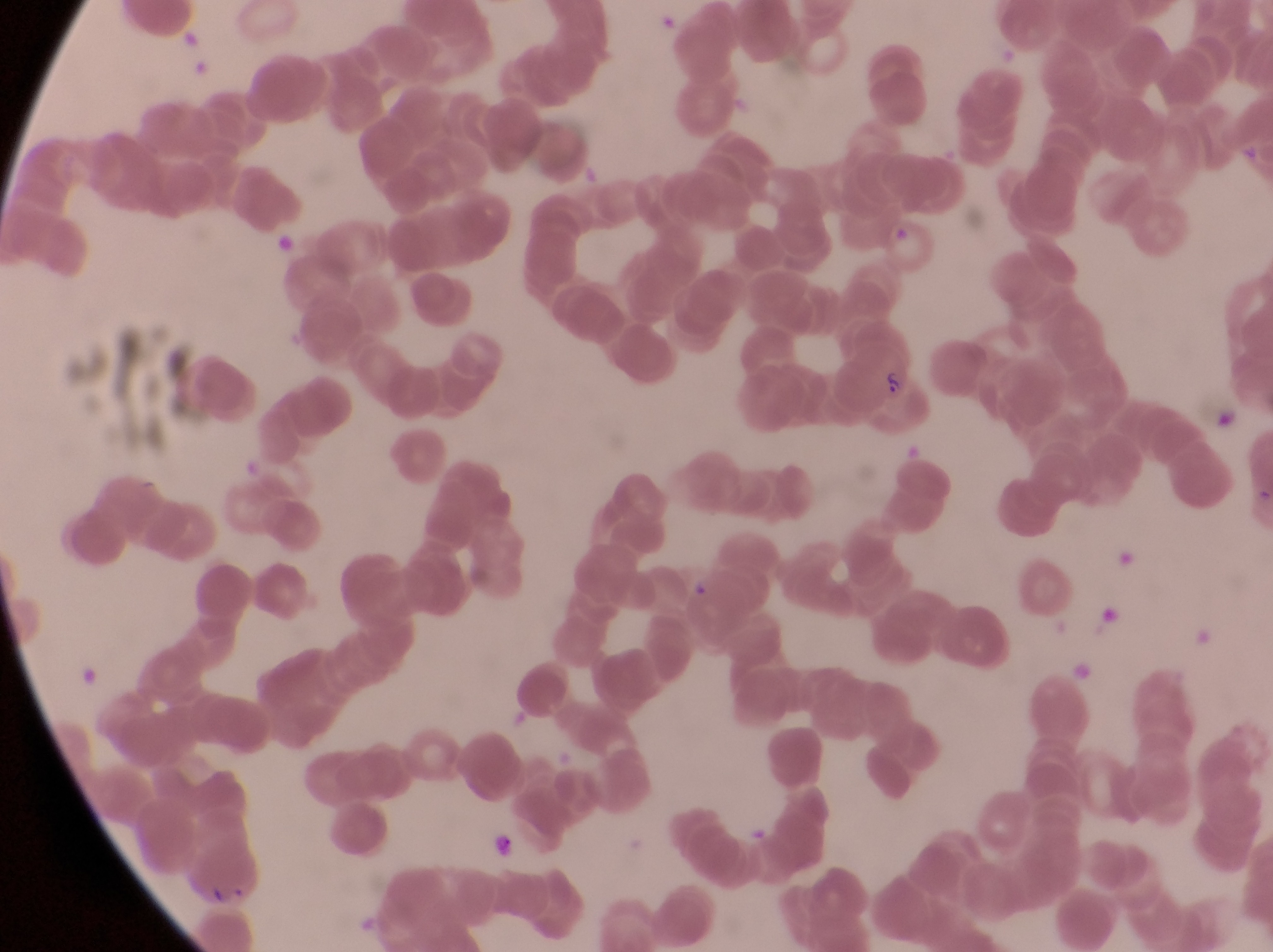

image size = 1273×952 pixels
preparation = thin blood smear
capture = smartphone photograph through the eyepiece of an Olympus CX-23 microscope
parasitised red blood cell locations = approximate bounding boxes as (left, top, right, bottom) in pixels: (839, 339, 927, 431), (1111, 543, 1143, 571), (1070, 658, 1098, 685), (176, 836, 265, 906)
magnification = 1000x
field of view = single
artifact (platelet-like body, stain precipitate, or debris) locations = approximate bounding boxes as (left, top, right, bottom) in pixels: (1100, 605, 1124, 634), (486, 826, 523, 861)
country = Uganda